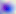
Toxoplasma gondii is shown. 400x magnification. Micrograph.